Assess the morphology of the erythrocytes.
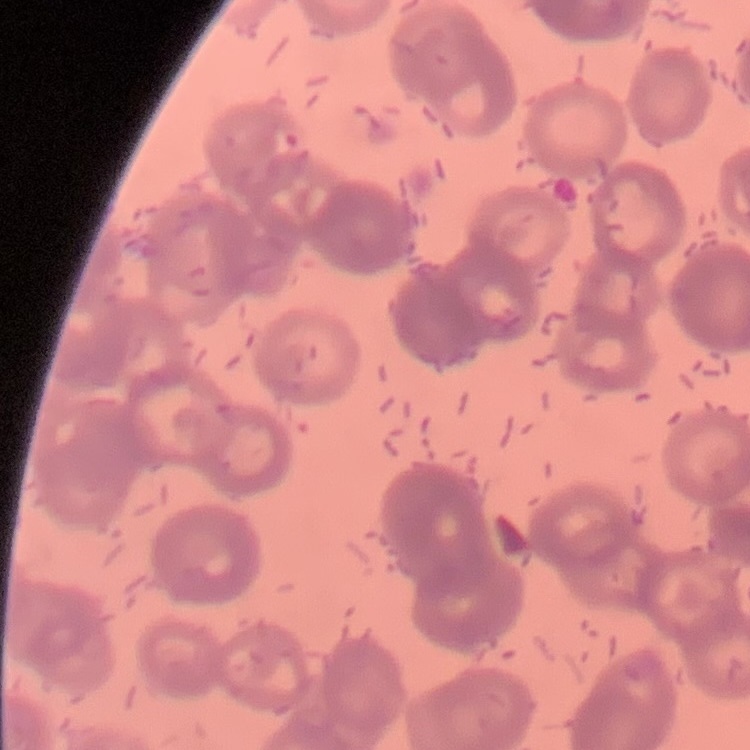
Rouleaux formation.

Summary:
  - Image type: one tile cut from a larger photomicrograph
  - Stain: Field's or Giemsa
  - Preparation: thin peripheral smear